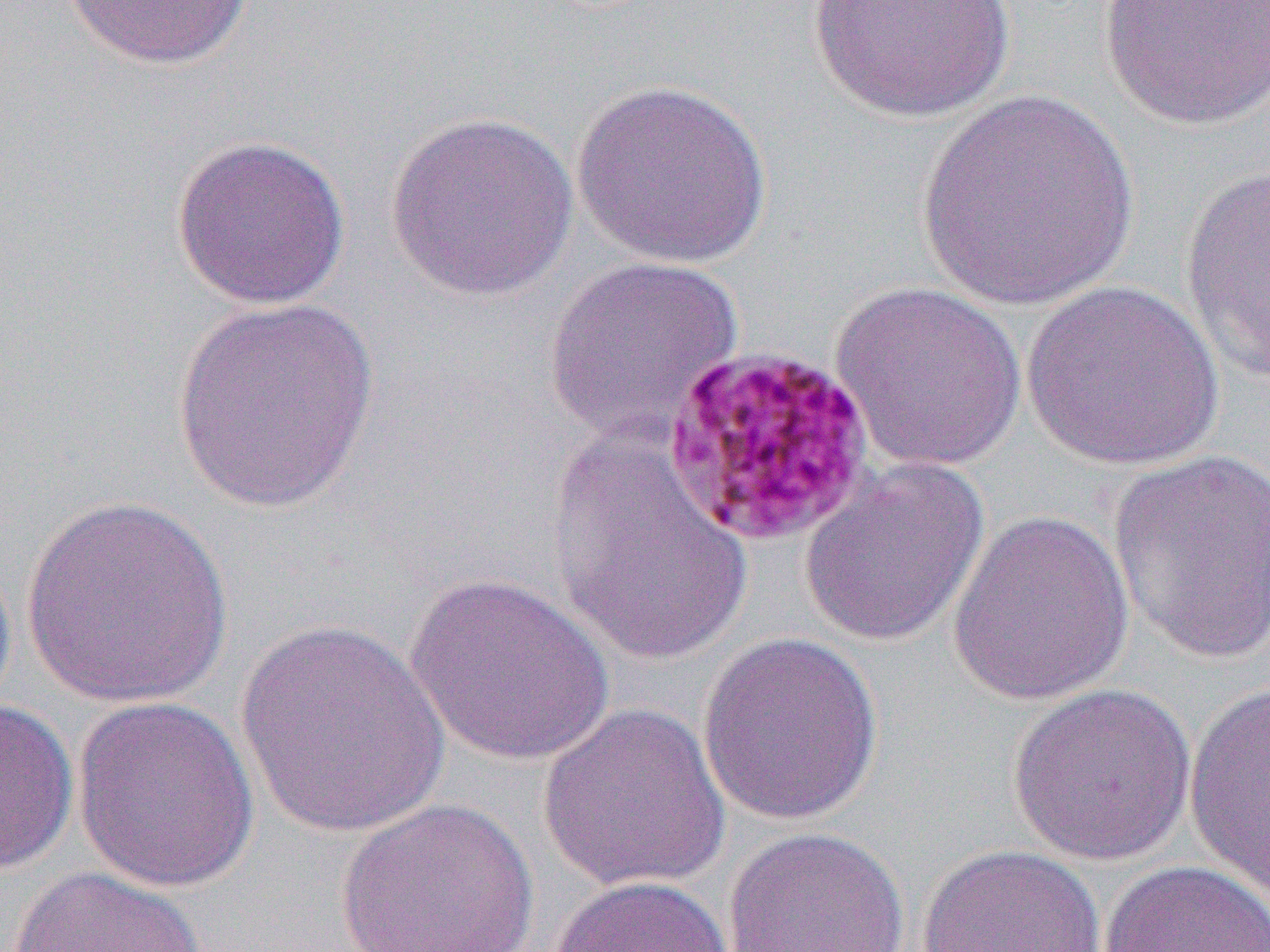
slide_level_diagnosis: Plasmodium malariae
field_of_view: single
image_size: 1270×952 pixels
modality: light microscopy
preparation: thin blood film
magnification: 1000x
uninfected_red_blood_cell_locations: 'approximate bounding boxes as (x1,y1)-(x2,y2) corner pairs in pixels: (63,0)-(256,70), (805,0)-(1021,123), (1098,0)-(1269,132), (571,78)-(774,268), (916,90)-(1140,313), (385,110)-(580,302), (170,134)-(351,310), (1179,160)-(1270,384), (542,255)-(745,444), (1021,279)-(1225,471), (831,281)-(1027,472), (171,299)-(382,516), (546,429)-(753,665), (1106,449)-(1270,665), (798,458)-(991,649), (21,495)-(234,709), (947,510)-(1135,706), (404,573)-(619,768), (233,619)-(452,838), (696,630)-(885,827), (1006,681)-(1198,867), (1183,681)-(1269,901), (69,695)-(261,894), (0,698)-(79,875), (536,701)-(732,895), (333,797)-(540,952), (721,826)-(911,952), (915,844)-(1108,952), (1099,860)-(1269,952), (9,866)-(211,952), (548,874)-(734,952)'